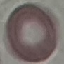
Summary:
  - Malaria status: uninfected
  - Preparation: thin blood smear
  - Stain: Giemsa
  - Image type: cell patch, automatically extracted from a larger field of view and resized to 64 × 64 pixels
  - Capture: smartphone through the microscope eyepiece